Report the malaria status of this cell.
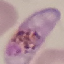

Parasitized.

Photographed with a smartphone camera at the microscope eyepiece. Automatically extracted cell patch, resized to 64 × 64 pixels. Thin blood smear. Giemsa-stained preparation.